Give the position of every leukocyte visible.
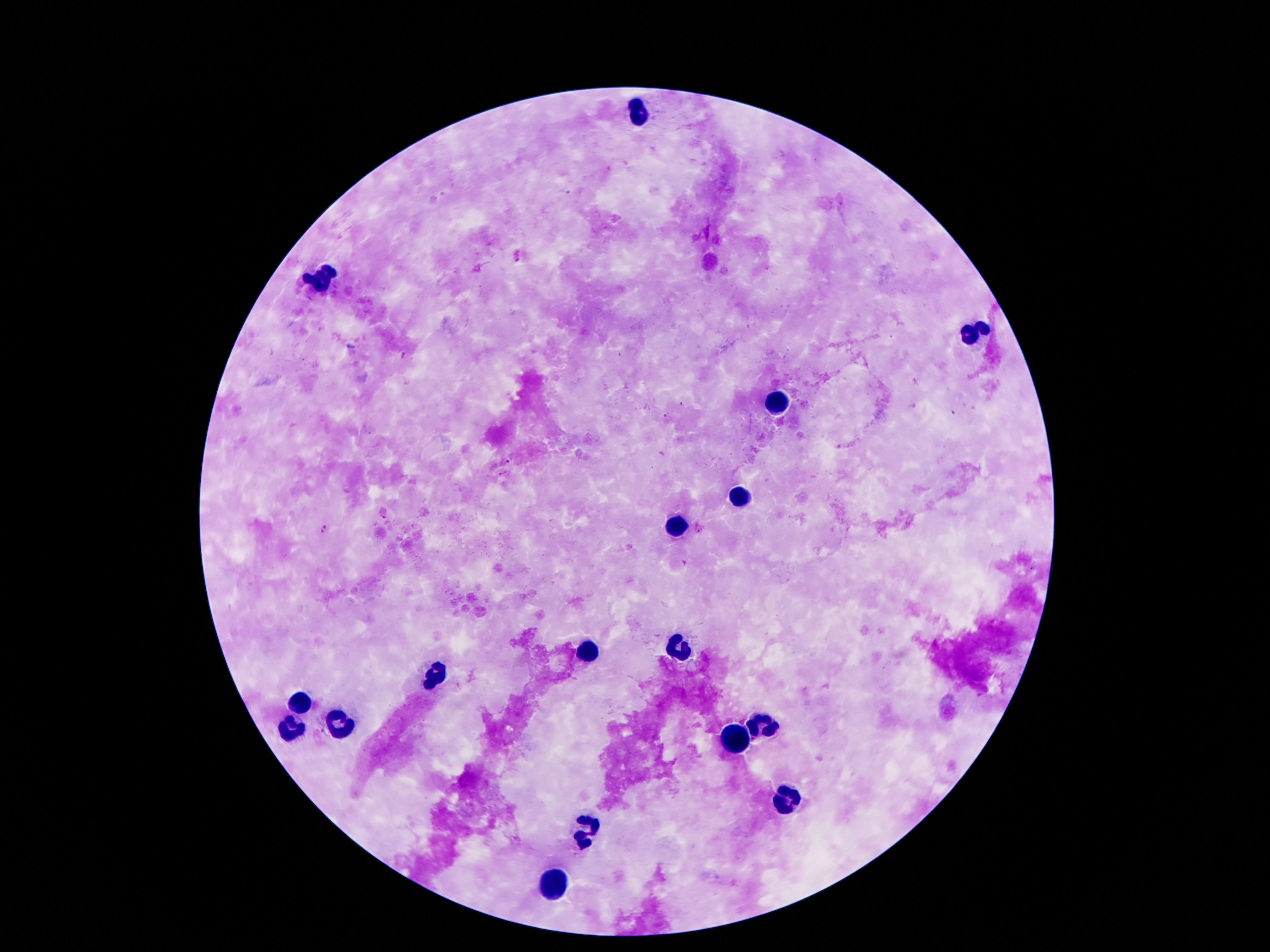
Approximate centers as {x, y} in pixels.
Leukocytes: {638, 112}, {331, 270}, {321, 282}, {981, 328}, {963, 336}, {781, 399}, {741, 495}, {676, 527}, {678, 645}, {588, 653}, {433, 674}, {298, 706}, {342, 725}, {766, 726}, {292, 731}, {735, 737}, {787, 802}, {584, 827}, {552, 888}.

preparation = thick peripheral-blood smear
patient malaria status = negative
image size = 1270×952 pixels
stain = Giemsa
capture = smartphone camera through the microscope eyepiece
field of view = one from this slide
magnification = 100x